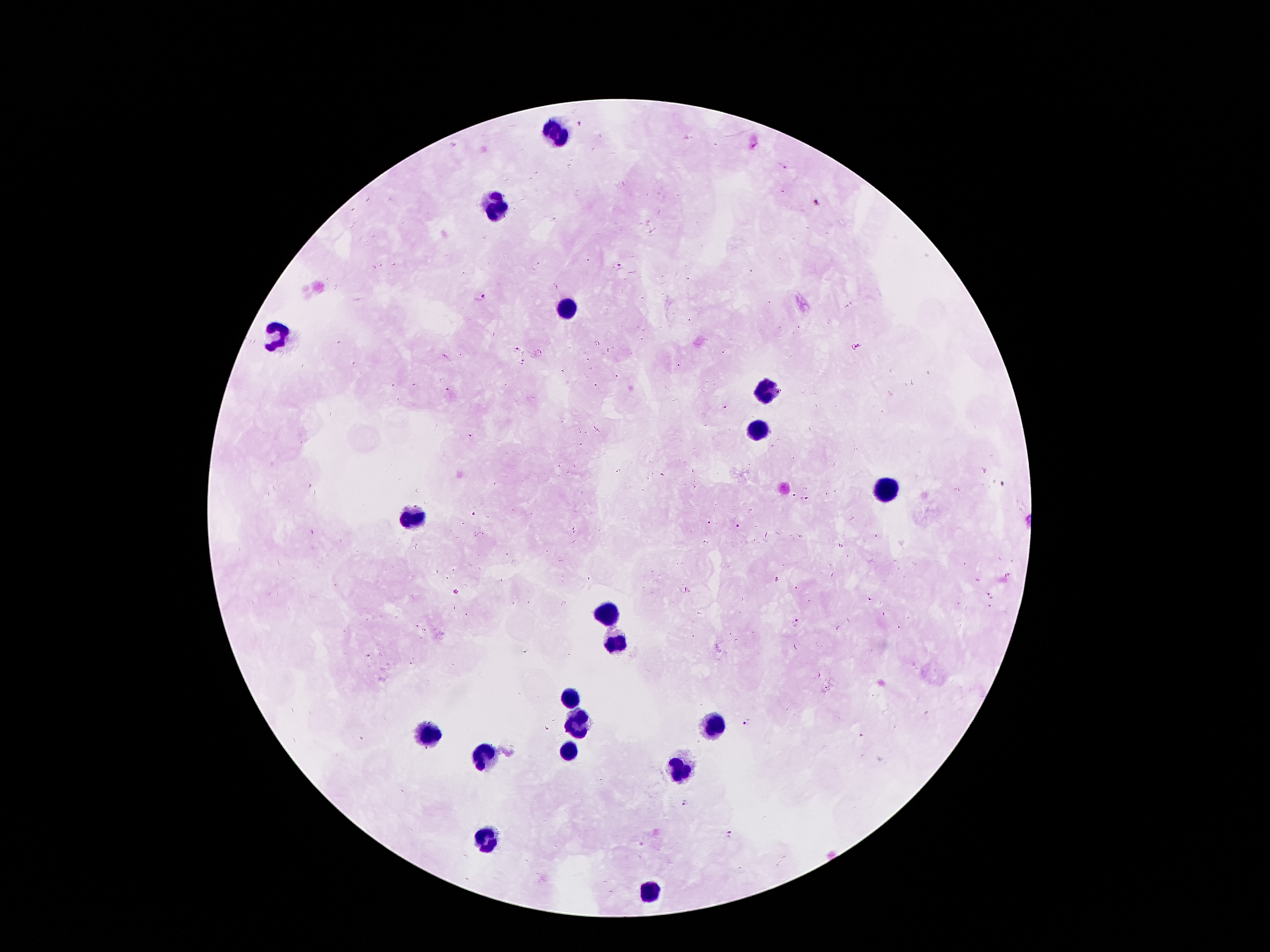

Approximate centers as [x, y] in pixels.
Summary:
  - Plasmodium parasite locations: [582, 124], [785, 169], [817, 202], [621, 266], [480, 297], [799, 328], [857, 347], [516, 350], [541, 351], [725, 352], [522, 362], [679, 365], [615, 376], [597, 384], [447, 389], [726, 408], [579, 432], [586, 433], [470, 435], [581, 444], [618, 471], [1003, 486], [472, 514], [708, 521], [739, 525], [778, 581], [683, 589], [456, 592], [989, 596], [871, 600], [796, 623], [417, 626], [425, 630], [525, 653], [368, 656], [816, 675], [745, 723], [685, 803], [728, 835]
  - Leukocyte locations: [553, 135], [494, 208], [571, 306], [278, 337], [766, 392], [757, 429], [884, 488], [419, 513], [607, 612], [616, 642], [571, 698], [576, 724], [712, 726], [430, 731], [483, 755], [682, 769], [487, 842], [650, 891]
  - Magnification: 100x
  - Patient malaria status: positive for Plasmodium falciparum
  - Capture: smartphone camera through the microscope eyepiece
  - Stain: Giemsa
  - Field of view: single
  - Image size: 1270×952 pixels
  - Preparation: thick peripheral-blood smear